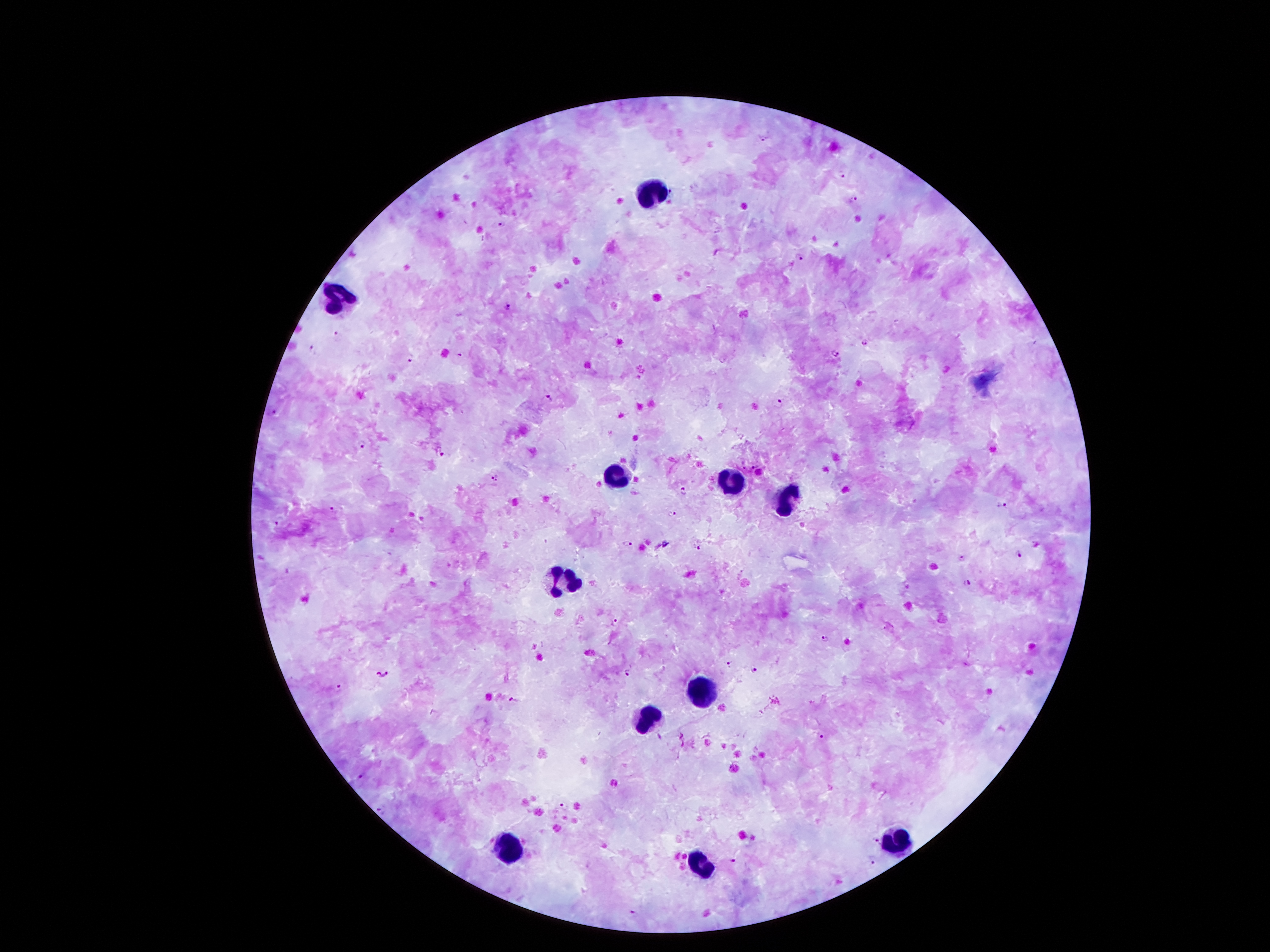

Approximate object centers, in pixels from the top-left corner.
Summary:
  - Malaria parasite locations: (x=765, y=136), (x=841, y=174), (x=853, y=199), (x=502, y=224), (x=801, y=258), (x=508, y=305), (x=338, y=334), (x=866, y=342), (x=312, y=348), (x=834, y=353), (x=458, y=355), (x=410, y=357), (x=548, y=399), (x=782, y=399), (x=274, y=411), (x=362, y=443), (x=443, y=452), (x=753, y=466), (x=494, y=479), (x=683, y=490), (x=1002, y=503), (x=333, y=507), (x=672, y=514), (x=279, y=520), (x=628, y=543), (x=698, y=546), (x=963, y=557), (x=1019, y=557), (x=968, y=582), (x=615, y=622), (x=824, y=637), (x=729, y=662), (x=753, y=670), (x=382, y=673), (x=628, y=673), (x=341, y=689), (x=512, y=699), (x=820, y=736), (x=360, y=774), (x=565, y=805), (x=382, y=809), (x=878, y=840), (x=734, y=860), (x=873, y=861), (x=633, y=913)
  - Leukocyte locations: (x=652, y=193), (x=337, y=292), (x=620, y=474), (x=732, y=485), (x=782, y=502), (x=564, y=586), (x=700, y=688), (x=645, y=718), (x=897, y=842), (x=507, y=848), (x=702, y=865)
  - Field of view: one from this slide
  - Magnification: 100x
  - Preparation: thick blood film
  - Capture: smartphone camera through the microscope eyepiece
  - Image size: 1270×952 pixels
  - Patient malaria status: positive for Plasmodium falciparum
  - Stain: Giemsa